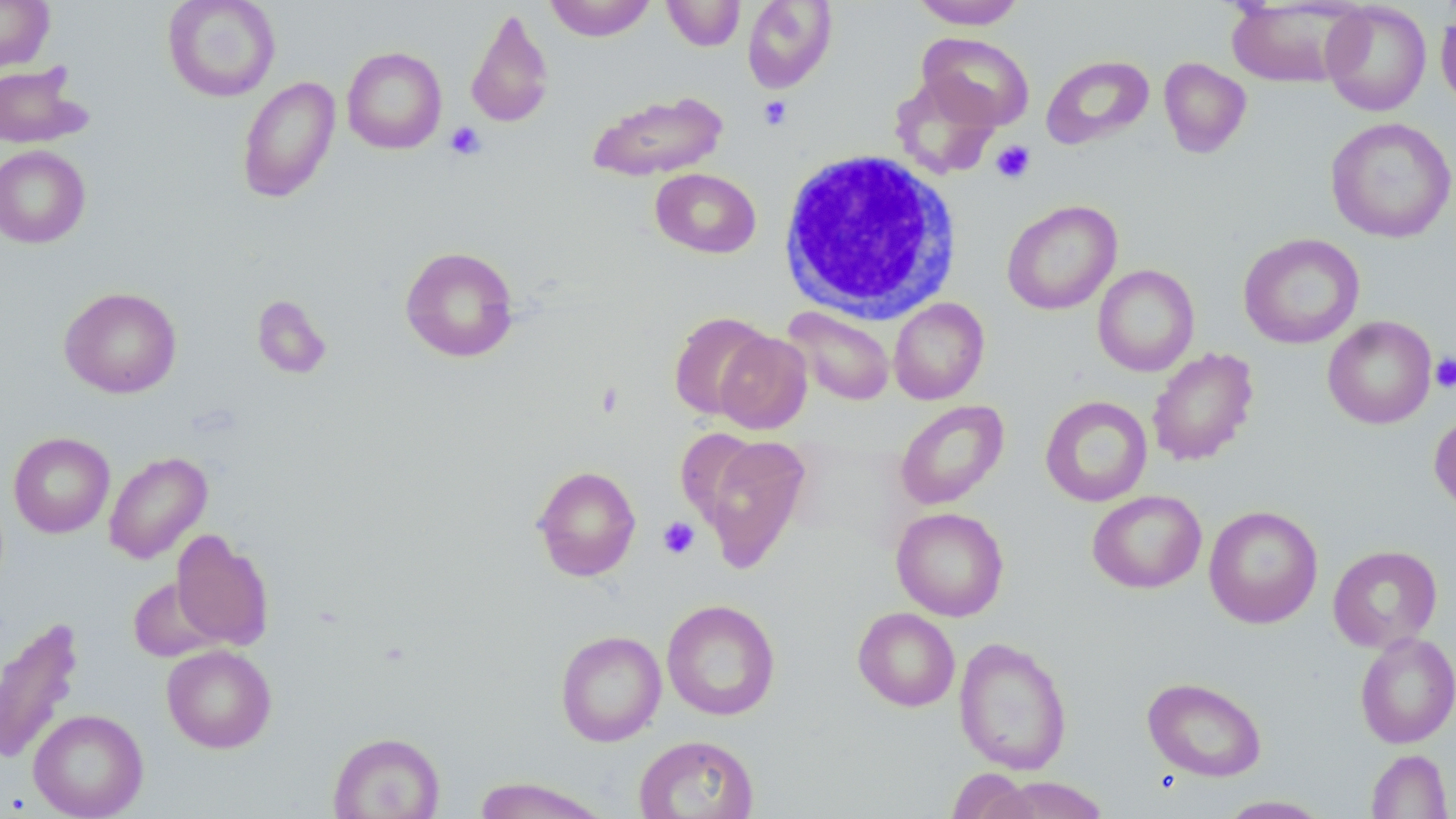

Summary:
  - Coordinate format: approximate bounding boxes as named x1/y1/x2/y2 corners in pixels
  - White blood cell locations: (x1=777, y1=148, x2=962, y2=323)
  - Platelet locations: (x1=759, y1=95, x2=793, y2=130), (x1=446, y1=122, x2=486, y2=160), (x1=991, y1=140, x2=1036, y2=184), (x1=1430, y1=353, x2=1456, y2=393), (x1=657, y1=516, x2=700, y2=559)
  - Uninfected red blood cell locations: (x1=0, y1=0, x2=54, y2=72), (x1=162, y1=0, x2=281, y2=102), (x1=543, y1=0, x2=656, y2=41), (x1=662, y1=0, x2=746, y2=51), (x1=742, y1=0, x2=837, y2=93), (x1=910, y1=0, x2=1027, y2=29), (x1=1226, y1=0, x2=1363, y2=89), (x1=1321, y1=1, x2=1432, y2=117), (x1=465, y1=7, x2=554, y2=130), (x1=1435, y1=8, x2=1456, y2=111), (x1=917, y1=32, x2=1035, y2=131), (x1=342, y1=46, x2=447, y2=154), (x1=1041, y1=55, x2=1154, y2=149), (x1=1158, y1=57, x2=1252, y2=158), (x1=0, y1=63, x2=90, y2=148), (x1=890, y1=73, x2=1001, y2=179), (x1=237, y1=76, x2=340, y2=203), (x1=588, y1=90, x2=728, y2=181), (x1=1325, y1=117, x2=1456, y2=243), (x1=0, y1=145, x2=91, y2=248), (x1=650, y1=168, x2=762, y2=259), (x1=1002, y1=199, x2=1122, y2=315), (x1=1238, y1=233, x2=1364, y2=349), (x1=400, y1=246, x2=519, y2=362), (x1=1092, y1=264, x2=1200, y2=377), (x1=59, y1=286, x2=182, y2=398), (x1=251, y1=295, x2=333, y2=379), (x1=889, y1=298, x2=989, y2=404), (x1=782, y1=307, x2=896, y2=406), (x1=668, y1=311, x2=775, y2=420), (x1=1322, y1=316, x2=1437, y2=429), (x1=713, y1=332, x2=812, y2=434), (x1=1147, y1=347, x2=1259, y2=466), (x1=1040, y1=396, x2=1153, y2=507), (x1=895, y1=400, x2=1009, y2=510), (x1=1429, y1=410, x2=1456, y2=515), (x1=9, y1=432, x2=114, y2=538), (x1=694, y1=434, x2=812, y2=572), (x1=104, y1=450, x2=213, y2=564), (x1=532, y1=465, x2=641, y2=581), (x1=1087, y1=490, x2=1206, y2=593), (x1=1204, y1=504, x2=1323, y2=629), (x1=891, y1=506, x2=1010, y2=621), (x1=170, y1=529, x2=274, y2=650), (x1=1328, y1=544, x2=1443, y2=653), (x1=128, y1=576, x2=222, y2=662), (x1=662, y1=599, x2=780, y2=720), (x1=853, y1=607, x2=960, y2=711), (x1=0, y1=616, x2=85, y2=766), (x1=555, y1=630, x2=667, y2=746), (x1=1355, y1=632, x2=1456, y2=748), (x1=953, y1=636, x2=1072, y2=775), (x1=162, y1=644, x2=276, y2=753), (x1=1142, y1=676, x2=1267, y2=782), (x1=28, y1=708, x2=148, y2=819), (x1=329, y1=731, x2=445, y2=819), (x1=633, y1=734, x2=760, y2=819), (x1=1367, y1=749, x2=1452, y2=818), (x1=947, y1=768, x2=1037, y2=818), (x1=987, y1=776, x2=1114, y2=818), (x1=473, y1=777, x2=612, y2=819), (x1=1216, y1=795, x2=1333, y2=818)
  - Slide-level diagnosis: no evidence of blood parasites
  - Modality: optical microscopy
  - Magnification: 1000x
  - Preparation: thin blood smear
  - Stain: May-Grünwald-Giemsa
  - Field of view: single
  - Image size: 1456×819 pixels